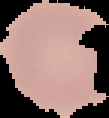
Image is 109×118 pixels. From a thin blood film. Segmented cell region on a black background. Result: no Plasmodium parasites detected.